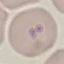
malaria status = uninfected
capture = smartphone through the microscope eyepiece
image type = automatically extracted cell patch, resized to 64 × 64 pixels
preparation = thin blood smear
stain = Giemsa